Locate every blood parasite and identify its species.
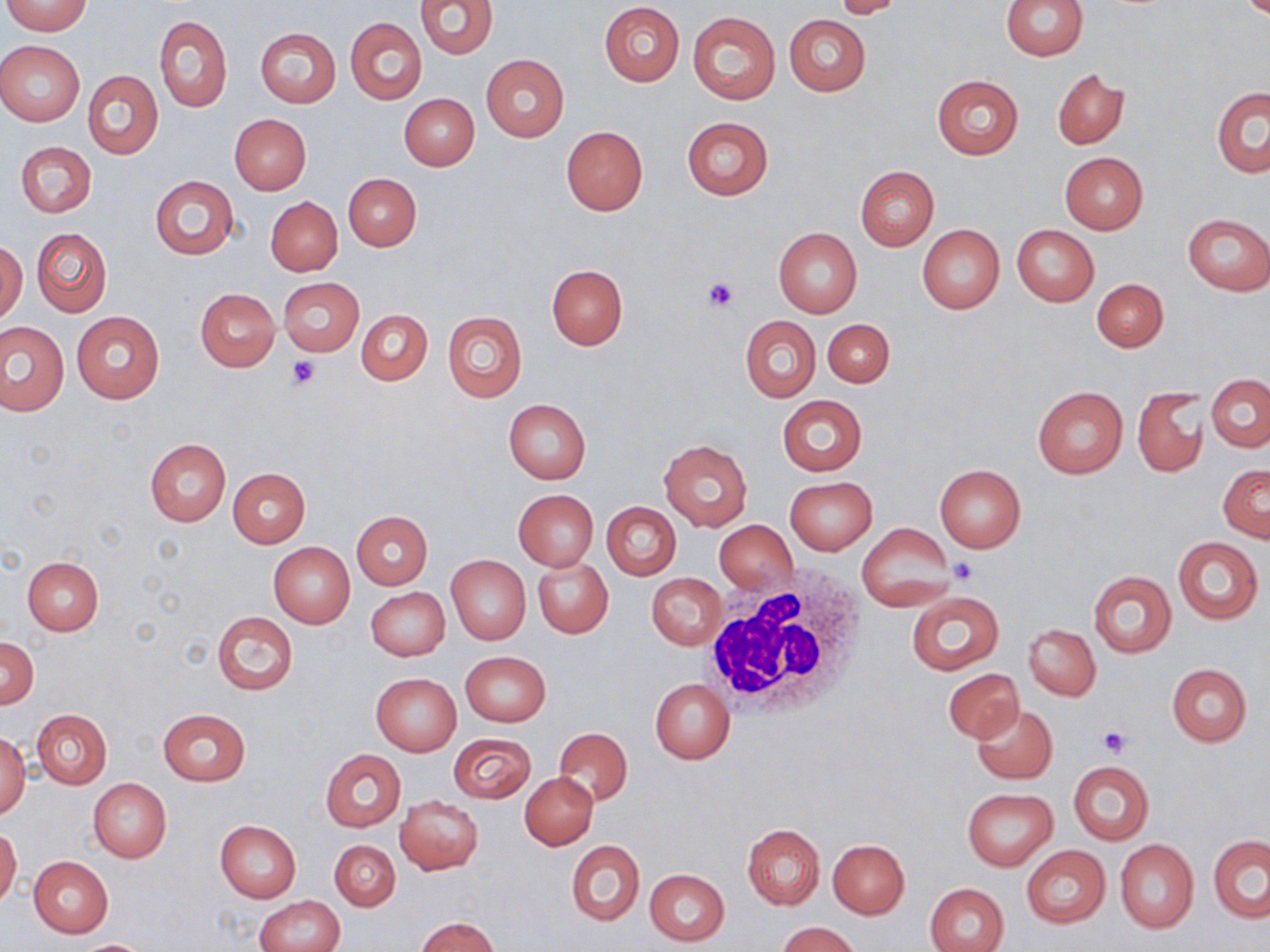

No blood parasites seen.

slide-level diagnosis = negative for blood parasites
image size = 1270×952 pixels
modality = light microscopy
platelet locations = approximate bounding boxes as (x1, y1, x2, y2) in pixels: (702, 278, 738, 313), (287, 355, 321, 389), (950, 559, 978, 585), (1099, 725, 1131, 757)
white blood cell locations = approximate bounding boxes as (x1, y1, x2, y2) in pixels: (698, 571, 873, 725)
uninfected red blood cell locations = approximate bounding boxes as (x1, y1, x2, y2) in pixels: (416, 0, 497, 60), (832, 0, 906, 18), (1002, 0, 1086, 60), (4, 1, 93, 35), (599, 2, 685, 86), (687, 12, 780, 103), (784, 14, 871, 96), (156, 15, 232, 112), (346, 18, 426, 104), (255, 27, 341, 107), (0, 40, 85, 126), (480, 54, 569, 140), (1053, 68, 1129, 149), (83, 71, 164, 160), (932, 74, 1024, 159), (1212, 86, 1270, 177), (400, 93, 479, 170), (230, 113, 311, 194), (681, 116, 773, 201), (561, 126, 648, 214), (15, 141, 96, 217), (1059, 152, 1148, 235), (855, 165, 938, 250), (344, 173, 421, 250), (149, 175, 239, 260), (266, 196, 343, 276), (1182, 214, 1270, 294), (1012, 224, 1099, 306), (917, 225, 1004, 314), (32, 228, 111, 317), (773, 228, 862, 318), (1, 241, 26, 324), (547, 264, 627, 349), (278, 277, 364, 356), (1092, 278, 1168, 351), (195, 288, 280, 371), (71, 309, 165, 405), (355, 309, 431, 385), (442, 310, 527, 403), (740, 315, 820, 402), (822, 318, 894, 387), (1, 322, 67, 416), (1205, 375, 1269, 451), (1033, 386, 1127, 478), (1133, 386, 1209, 478), (777, 395, 867, 476), (503, 399, 590, 484), (659, 437, 753, 531), (145, 439, 231, 525), (934, 464, 1026, 552), (1218, 464, 1269, 542), (228, 467, 310, 547), (784, 477, 876, 554), (513, 490, 598, 571), (602, 502, 680, 578), (351, 510, 433, 589), (714, 520, 797, 594), (855, 522, 956, 612), (1173, 535, 1263, 624), (269, 543, 355, 628), (446, 555, 530, 644), (22, 557, 104, 634), (532, 557, 612, 638), (1088, 570, 1176, 657), (646, 573, 726, 650), (367, 588, 450, 660), (907, 590, 1004, 676), (212, 611, 297, 695), (1023, 624, 1099, 700), (1, 638, 39, 707), (461, 651, 550, 726), (1166, 663, 1252, 746), (944, 668, 1024, 743), (371, 673, 461, 756), (650, 679, 734, 764), (972, 702, 1057, 784), (158, 708, 251, 786), (32, 709, 111, 788), (553, 727, 632, 806), (448, 732, 537, 804), (0, 733, 30, 818), (320, 750, 406, 831), (1068, 761, 1153, 845), (520, 772, 598, 849), (88, 778, 171, 863), (962, 788, 1057, 869), (395, 796, 483, 875), (215, 819, 301, 903), (742, 823, 824, 909), (0, 827, 21, 907), (1209, 835, 1270, 922), (329, 839, 401, 911), (828, 839, 909, 918), (567, 840, 643, 925), (1115, 840, 1198, 932), (1022, 845, 1110, 927), (28, 855, 113, 936), (644, 869, 729, 946), (925, 882, 1009, 952), (253, 895, 344, 952), (414, 917, 500, 951), (776, 921, 863, 952), (73, 939, 157, 952)
stain = May-Grünwald-Giemsa
preparation = thin blood smear
magnification = 1000x
field of view = one of a larger specimen